Locate every white blood cell.
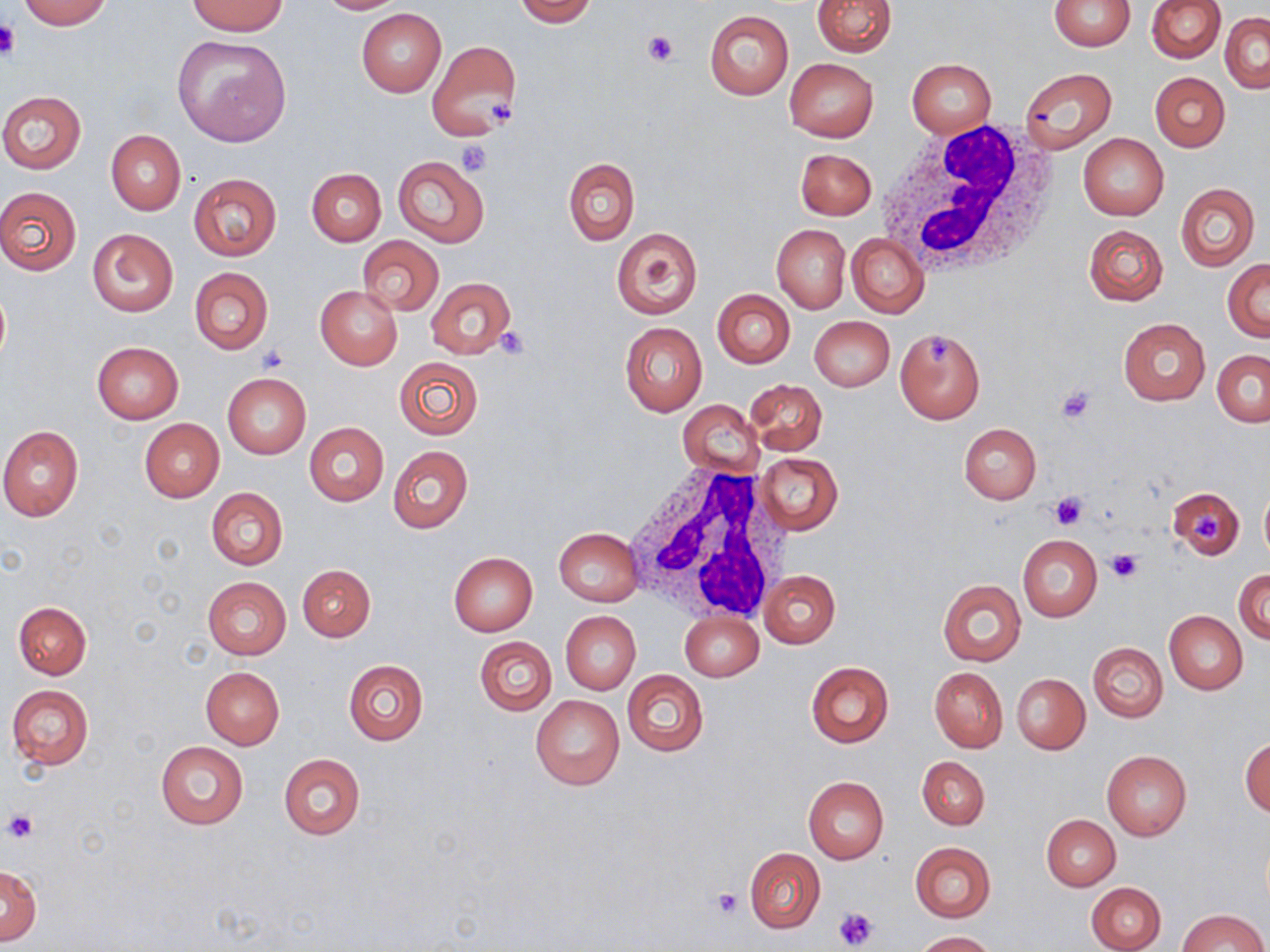

Approximate bounding boxes as (x1, y1, x2, y2) in pixels.
White blood cells: (874, 121, 1064, 283), (625, 464, 787, 620).

slide_level_diagnosis: negative for blood parasites
magnification: 1000x
uninfected_red_blood_cell_locations: 'approximate bounding boxes as (x1, y1, x2, y2) in pixels: (17, 0, 113, 30), (314, 0, 404, 14), (514, 0, 598, 26), (812, 0, 895, 57), (1049, 0, 1135, 52), (1146, 0, 1226, 63), (188, 1, 287, 36), (357, 9, 445, 96), (704, 10, 793, 100), (1221, 12, 1269, 93), (172, 35, 291, 146), (427, 40, 520, 140), (784, 57, 878, 142), (908, 60, 996, 136), (1020, 66, 1116, 153), (1150, 72, 1230, 151), (0, 91, 87, 173), (106, 130, 186, 215), (1078, 133, 1169, 220), (795, 149, 876, 220), (392, 155, 490, 248), (562, 157, 639, 247), (306, 168, 385, 246), (188, 174, 281, 260), (1175, 182, 1260, 272), (0, 185, 82, 276), (1083, 224, 1169, 306), (772, 225, 849, 313), (87, 228, 178, 317), (611, 228, 701, 319), (846, 233, 929, 318), (357, 236, 444, 315), (1224, 259, 1270, 340), (189, 267, 273, 355), (425, 278, 516, 360), (315, 286, 403, 370), (713, 290, 795, 368), (810, 316, 895, 391), (1118, 318, 1209, 406), (620, 323, 707, 416), (896, 328, 986, 424), (91, 342, 183, 423), (1212, 349, 1270, 427), (392, 357, 485, 441), (222, 373, 311, 458), (746, 379, 827, 455), (677, 400, 763, 478), (139, 418, 224, 503), (304, 423, 389, 506), (959, 423, 1041, 504), (0, 425, 83, 521), (388, 445, 473, 533), (755, 453, 841, 536), (1168, 484, 1246, 560), (1259, 484, 1270, 564), (206, 487, 288, 570), (553, 527, 643, 606), (1018, 534, 1101, 622), (448, 552, 538, 636), (298, 564, 375, 640), (760, 569, 839, 647), (1234, 569, 1270, 643), (203, 577, 292, 660), (937, 580, 1026, 666), (12, 601, 91, 679), (561, 611, 640, 694), (680, 611, 763, 682), (1165, 611, 1247, 693), (474, 636, 556, 715), (1088, 642, 1167, 722), (344, 660, 428, 745), (806, 660, 894, 748), (200, 666, 285, 749), (929, 666, 1008, 752), (623, 670, 708, 756), (1012, 673, 1089, 754), (7, 685, 94, 769), (531, 693, 624, 790), (1241, 736, 1269, 816), (154, 741, 249, 830), (1101, 750, 1191, 842), (278, 754, 365, 840), (917, 756, 990, 829), (802, 776, 888, 864), (1042, 814, 1121, 890), (910, 842, 996, 922), (745, 848, 825, 933), (0, 863, 41, 946), (1087, 881, 1165, 951), (1177, 908, 1268, 952), (914, 931, 996, 951)'
modality: light microscopy
stain: May-Grünwald-Giemsa
field_of_view: one of a larger specimen
platelet_locations: 'approximate bounding boxes as (x1, y1, x2, y2) in pixels: (0, 21, 20, 62), (645, 30, 678, 67), (486, 98, 518, 127), (457, 140, 491, 175), (494, 327, 531, 360), (257, 347, 288, 373), (1056, 385, 1097, 423), (1049, 491, 1087, 530), (1193, 513, 1223, 543), (1105, 549, 1144, 585), (4, 809, 36, 844), (710, 886, 744, 918), (833, 906, 878, 950)'
preparation: thin blood film
image_size: 1270×952 pixels